Classify this cell by malaria status.
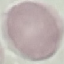

It is uninfected.

stain = Giemsa
capture = smartphone camera at the microscope eyepiece
preparation = thin smear
image type = automatically extracted cell patch, resized to 64 × 64 pixels